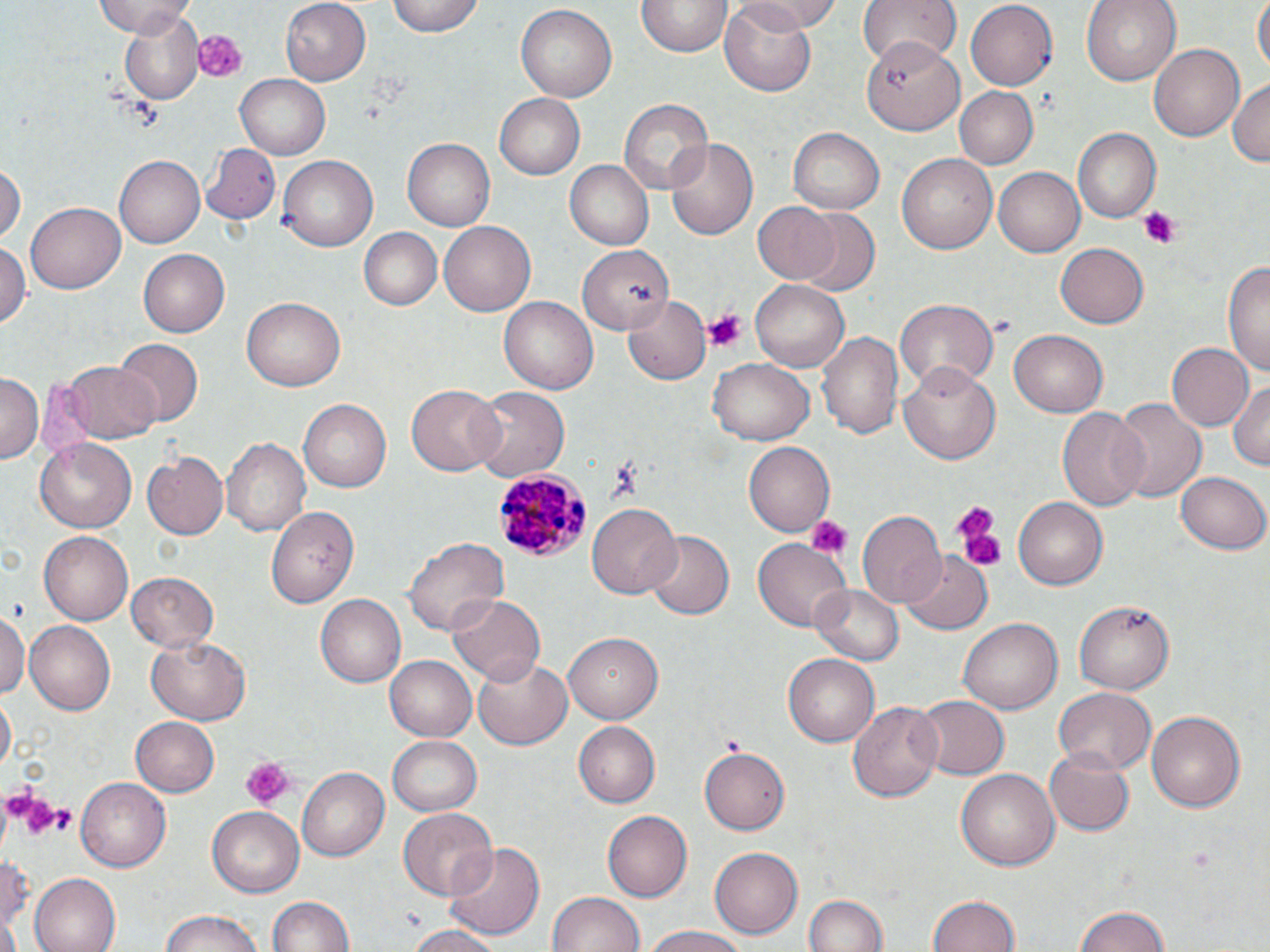
Summary:
  - Coordinate format: approximate bounding boxes as (x1, y1, x2, y2) in pixels
  - Plasmodium malariae-infected red blood cell locations: (492, 466, 589, 563)
  - Platelet locations: (189, 28, 248, 83), (1136, 206, 1182, 248), (701, 308, 748, 352), (950, 501, 1001, 569), (805, 514, 851, 560), (239, 758, 291, 809), (5, 785, 68, 843), (38, 800, 78, 838)
  - Uninfected red blood cell locations: (93, 0, 197, 38), (279, 0, 370, 85), (388, 0, 483, 37), (733, 0, 842, 33), (1082, 0, 1180, 85), (1251, 0, 1270, 75), (639, 1, 729, 58), (860, 1, 961, 69), (963, 2, 1058, 90), (721, 3, 816, 93), (515, 4, 618, 101), (116, 11, 208, 103), (864, 37, 963, 135), (1151, 43, 1244, 141), (235, 72, 332, 159), (1227, 77, 1270, 170), (953, 86, 1036, 169), (495, 92, 590, 180), (619, 98, 712, 196), (787, 129, 883, 213), (1072, 129, 1159, 221), (666, 137, 758, 240), (403, 139, 494, 231), (203, 143, 281, 225), (895, 153, 998, 255), (115, 155, 209, 248), (277, 156, 376, 252), (564, 160, 654, 251), (0, 161, 24, 246), (994, 167, 1085, 256), (24, 200, 125, 295), (752, 202, 842, 284), (793, 208, 880, 297), (438, 221, 534, 316), (359, 228, 442, 311), (0, 240, 29, 331), (1056, 241, 1149, 327), (578, 245, 674, 332), (137, 248, 230, 337), (1223, 259, 1270, 376), (751, 281, 849, 372), (624, 293, 713, 383), (242, 297, 343, 391), (499, 297, 596, 393), (894, 299, 998, 391), (1010, 330, 1107, 417), (818, 331, 903, 440), (111, 340, 200, 427), (1167, 342, 1254, 432), (707, 358, 814, 445), (61, 359, 160, 443), (900, 363, 1003, 463), (0, 375, 41, 462), (1228, 378, 1270, 471), (405, 384, 503, 475), (468, 386, 567, 481), (1111, 397, 1207, 503), (297, 399, 391, 491), (1056, 407, 1149, 510), (221, 438, 311, 537), (35, 439, 136, 533), (741, 443, 834, 537), (143, 452, 229, 539), (1176, 470, 1270, 554), (1014, 499, 1107, 591), (587, 503, 681, 598), (267, 508, 360, 606), (856, 512, 947, 610), (39, 531, 133, 625), (644, 531, 733, 620), (403, 536, 508, 636), (753, 540, 849, 631), (901, 550, 992, 633), (125, 572, 220, 652), (810, 581, 908, 666), (314, 595, 406, 688), (449, 595, 545, 683), (1073, 600, 1174, 696), (0, 612, 29, 697), (959, 615, 1062, 710), (23, 620, 116, 715), (562, 633, 661, 723), (147, 636, 250, 724), (783, 653, 879, 746), (473, 654, 573, 749), (386, 656, 476, 741), (1053, 688, 1155, 778), (1, 693, 16, 774), (913, 694, 1008, 780), (848, 700, 942, 802), (1146, 709, 1247, 813), (131, 716, 221, 797), (574, 722, 660, 808), (387, 734, 483, 815), (699, 746, 789, 834), (1044, 746, 1134, 836), (295, 768, 390, 862), (956, 768, 1059, 872), (74, 778, 171, 871), (209, 806, 304, 896), (397, 807, 497, 900), (603, 811, 691, 901), (442, 839, 547, 943), (0, 846, 37, 945), (709, 846, 803, 939), (29, 874, 120, 952), (546, 890, 643, 952), (802, 890, 887, 952), (267, 895, 354, 951), (925, 895, 1022, 952), (1071, 904, 1173, 952), (159, 911, 266, 952), (401, 924, 506, 952), (639, 926, 753, 952)
  - Slide-level diagnosis: Plasmodium malariae
  - Stain: May-Grünwald-Giemsa
  - Magnification: 1000x
  - Modality: light microscopy
  - Field of view: single
  - Preparation: thin blood smear
  - Image size: 1270×952 pixels